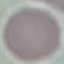
malaria_status: uninfected
image_type: cell patch, automatically extracted from a larger field of view and resized to 64 × 64 pixels
capture: smartphone through the microscope eyepiece
preparation: thin blood smear
stain: Giemsa